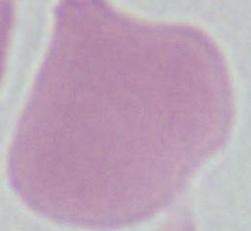
magnification: 1000x
modality: photomicrograph
identification: erythrocyte